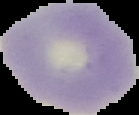

{
  "image_size": "139×115 pixels",
  "result": "no malaria parasites detected",
  "image_type": "cell region segmented out of the field of view; surrounding area masked to black",
  "preparation": "thin blood smear"
}